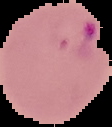 Segmented cell region on a black background. Result: malaria parasites detected. Image is 112×127 pixels. From a thin blood film.